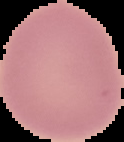
Summary:
  - Image type: segmented cell region on a black background
  - Preparation: thin blood smear
  - Malaria status: uninfected
  - Image size: 124×142 pixels